Name the cell type shown.
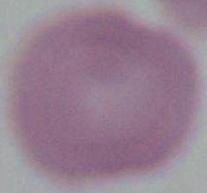
This is an erythrocyte.

Summary:
  - Modality: micrograph
  - Magnification: 1000x